Point out each malaria parasite and each leukocyte.
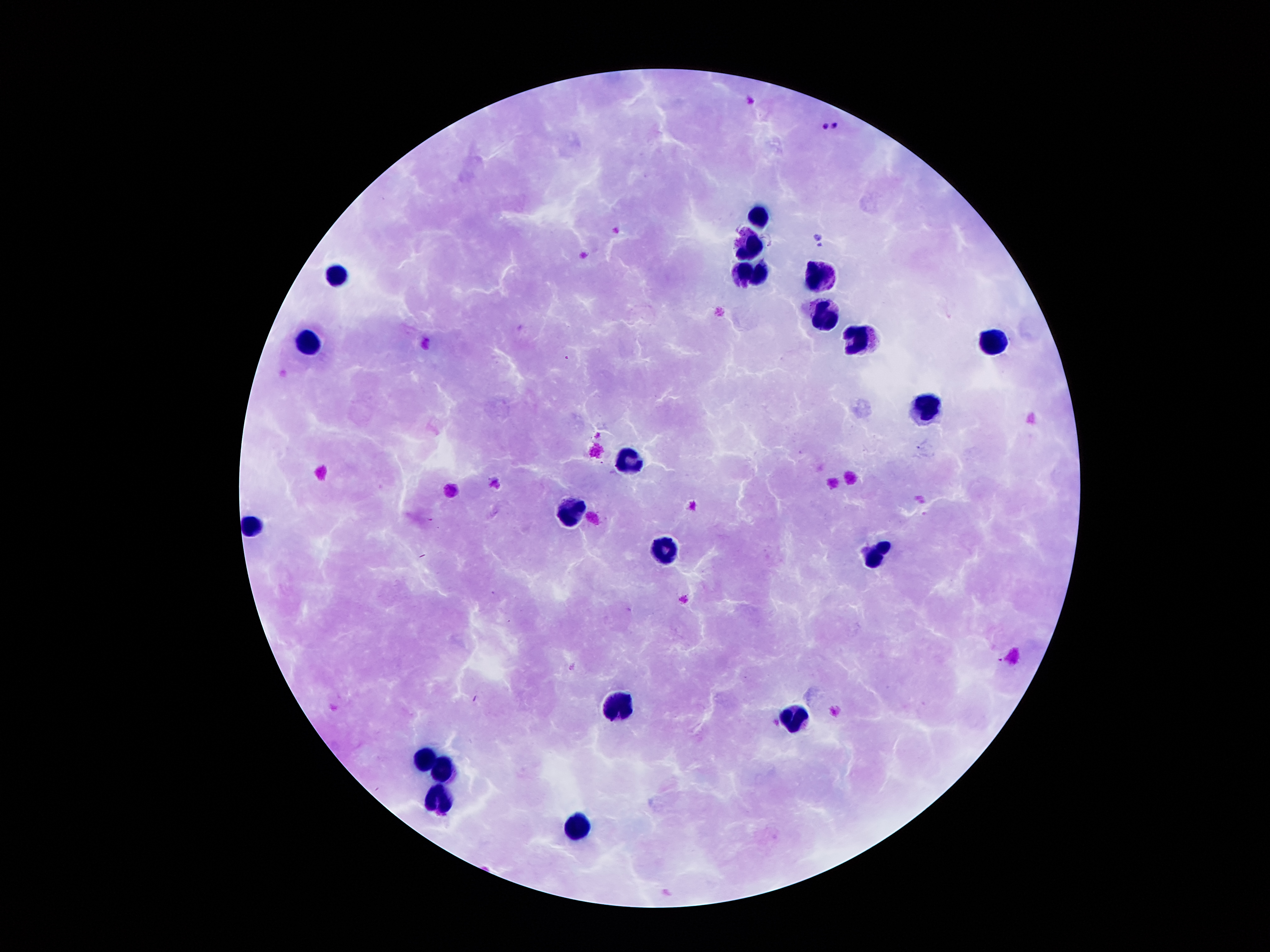
Approximate object centers, in pixels from the top-left corner.
Malaria parasites: (x=837, y=126), (x=825, y=128), (x=818, y=236), (x=819, y=246), (x=567, y=357).
Leukocytes: (x=759, y=218), (x=749, y=244), (x=759, y=270), (x=342, y=274), (x=822, y=274), (x=824, y=316), (x=857, y=338), (x=994, y=341), (x=306, y=343), (x=923, y=410), (x=631, y=459), (x=571, y=514), (x=255, y=526), (x=664, y=551), (x=877, y=557), (x=615, y=707), (x=791, y=718), (x=426, y=756), (x=445, y=769), (x=440, y=800), (x=577, y=826).

stain = Giemsa
preparation = thick blood film
capture = smartphone through the microscope eyepiece
magnification = 100x
field of view = single
image size = 1270×952 pixels
patient malaria status = positive for Plasmodium falciparum